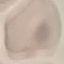

Summary:
  - Result: no malaria parasites detected
  - Stain: Giemsa
  - Capture: smartphone through the microscope eyepiece
  - Image type: cell patch, automatically extracted from a larger field of view and resized to 64 × 64 pixels
  - Preparation: thin blood film